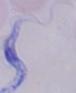 Photomicrograph. A trypanosome is shown. Captured at 1000x magnification.